Classify this cell by malaria status.
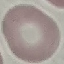

Uninfected.

Thin blood film. Automatically extracted cell patch, resized to 64 × 64 pixels. Acquired by smartphone through the microscope eyepiece. Giemsa stain.